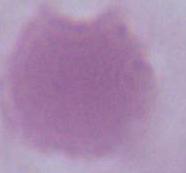
1000x magnification. A red blood cell is shown. Photomicrograph.